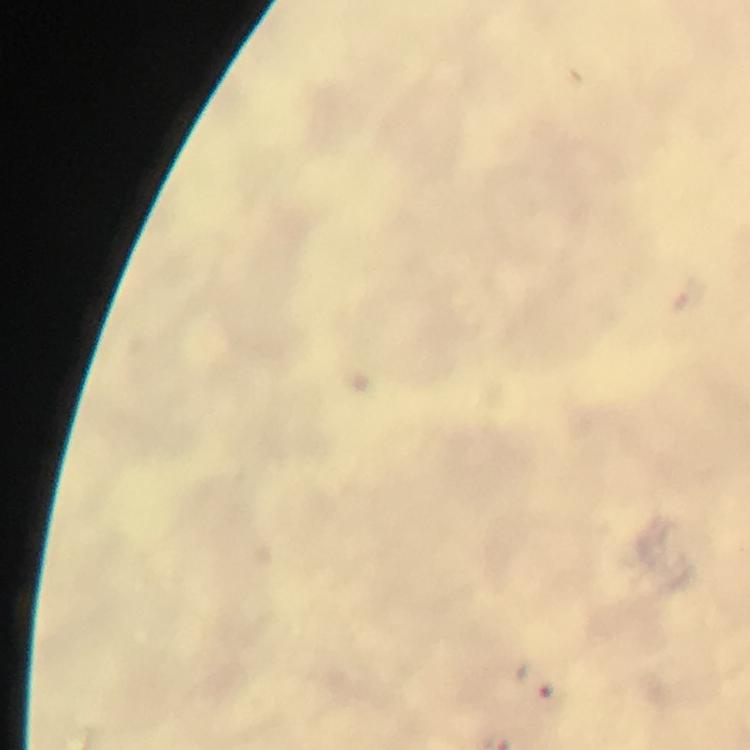
immersion oil = used
capture = smartphone camera through the microscope
Plasmodium parasite locations = approximate object centers, in pixels from the top-left corner: (x=533, y=683)
stain = Giemsa
magnification = 100x
preparation = thick blood film
context = from a diagnostic examination for malaria
image size = 750×750 pixels
cropped from = one field of view